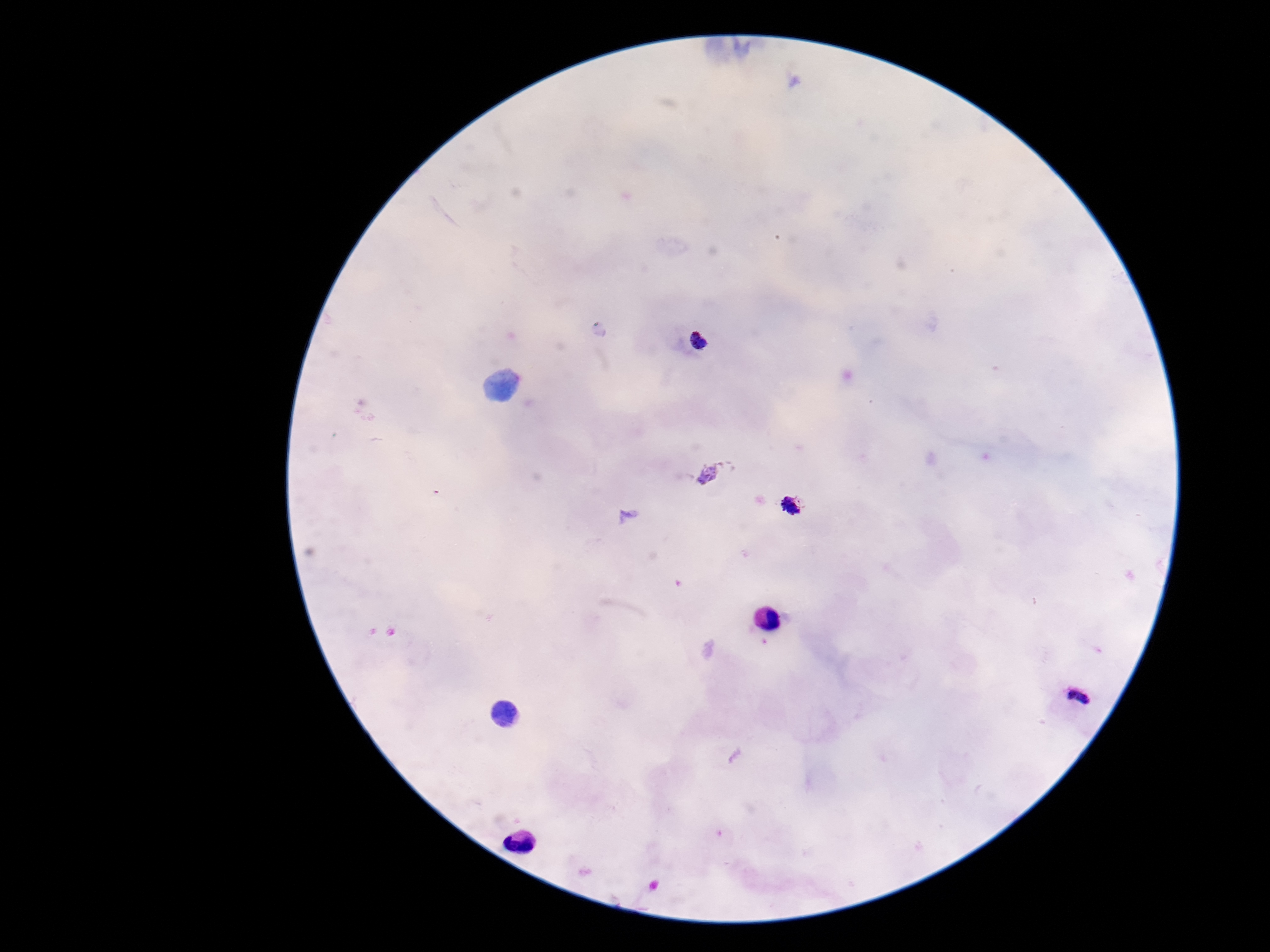
Approximate centers as [x, y] in pixels. Plasmodium parasite locations: [698, 340], [792, 506], [1079, 699]. Giemsa-stained preparation. Image is 1270×952 pixels. 100x magnification. Patient malaria status: infected. Thick blood film. Photographed through the microscope eyepiece with a smartphone camera. Single field of view.